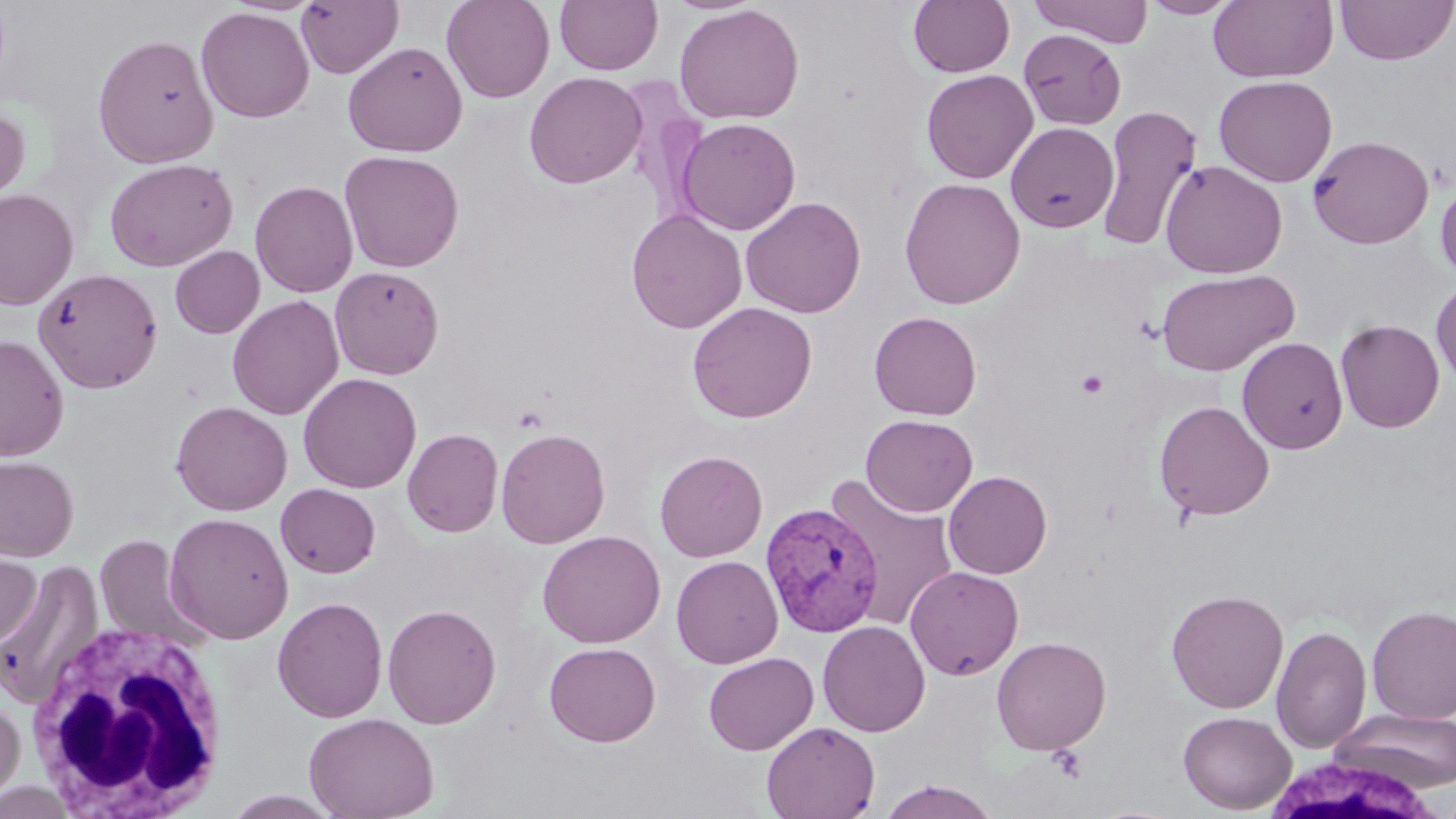
{
  "slide_level_diagnosis": "Plasmodium vivax",
  "uninfected_red_blood_cell_locations": "approximate bounding boxes as named x1/y1/x2/y2 corners in pixels: (x1=296, y1=0, x2=404, y2=79), (x1=441, y1=0, x2=554, y2=103), (x1=554, y1=0, x2=663, y2=75), (x1=908, y1=0, x2=1016, y2=78), (x1=1028, y1=0, x2=1153, y2=46), (x1=1138, y1=0, x2=1243, y2=19), (x1=1208, y1=0, x2=1338, y2=84), (x1=1334, y1=0, x2=1456, y2=66), (x1=674, y1=4, x2=804, y2=125), (x1=196, y1=8, x2=315, y2=123), (x1=1018, y1=28, x2=1126, y2=130), (x1=92, y1=33, x2=219, y2=168), (x1=343, y1=41, x2=468, y2=157), (x1=921, y1=68, x2=1038, y2=184), (x1=524, y1=71, x2=647, y2=189), (x1=1214, y1=75, x2=1337, y2=187), (x1=0, y1=101, x2=30, y2=211), (x1=1096, y1=104, x2=1202, y2=252), (x1=676, y1=117, x2=801, y2=236), (x1=1006, y1=121, x2=1119, y2=233), (x1=1307, y1=134, x2=1434, y2=249), (x1=339, y1=150, x2=464, y2=273), (x1=104, y1=157, x2=238, y2=272), (x1=1160, y1=159, x2=1287, y2=279), (x1=899, y1=177, x2=1026, y2=310), (x1=1435, y1=177, x2=1456, y2=285), (x1=250, y1=180, x2=359, y2=298), (x1=0, y1=188, x2=79, y2=310), (x1=740, y1=196, x2=866, y2=318), (x1=626, y1=209, x2=747, y2=334), (x1=170, y1=245, x2=265, y2=338), (x1=329, y1=265, x2=444, y2=380), (x1=34, y1=267, x2=162, y2=393), (x1=1156, y1=269, x2=1298, y2=377), (x1=1431, y1=280, x2=1456, y2=388), (x1=227, y1=295, x2=344, y2=420), (x1=687, y1=301, x2=818, y2=424), (x1=869, y1=311, x2=982, y2=420), (x1=1335, y1=318, x2=1445, y2=433), (x1=0, y1=334, x2=69, y2=460), (x1=1237, y1=336, x2=1348, y2=454), (x1=298, y1=372, x2=422, y2=493), (x1=170, y1=400, x2=293, y2=516), (x1=1154, y1=400, x2=1275, y2=521), (x1=861, y1=414, x2=978, y2=517), (x1=402, y1=427, x2=503, y2=537), (x1=495, y1=427, x2=610, y2=548), (x1=654, y1=450, x2=768, y2=562), (x1=0, y1=454, x2=79, y2=562), (x1=943, y1=471, x2=1052, y2=579), (x1=823, y1=474, x2=960, y2=631), (x1=275, y1=483, x2=381, y2=578), (x1=164, y1=512, x2=294, y2=644), (x1=537, y1=530, x2=666, y2=648), (x1=93, y1=534, x2=208, y2=650), (x1=0, y1=546, x2=41, y2=650), (x1=671, y1=555, x2=783, y2=668), (x1=1, y1=559, x2=104, y2=709), (x1=905, y1=565, x2=1024, y2=681), (x1=1166, y1=589, x2=1289, y2=713), (x1=272, y1=596, x2=389, y2=723), (x1=382, y1=603, x2=501, y2=729), (x1=1367, y1=605, x2=1456, y2=723), (x1=817, y1=620, x2=931, y2=737), (x1=1271, y1=625, x2=1371, y2=754), (x1=991, y1=636, x2=1111, y2=755), (x1=544, y1=642, x2=661, y2=747), (x1=703, y1=651, x2=819, y2=755), (x1=0, y1=693, x2=25, y2=808), (x1=1332, y1=708, x2=1456, y2=792), (x1=1178, y1=710, x2=1296, y2=814), (x1=304, y1=712, x2=439, y2=819), (x1=762, y1=721, x2=880, y2=819), (x1=876, y1=781, x2=1001, y2=818), (x1=223, y1=790, x2=343, y2=818)",
  "preparation": "thin blood smear",
  "white_blood_cell_locations": "approximate bounding boxes as named x1/y1/x2/y2 corners in pixels: (x1=26, y1=618, x2=230, y2=818), (x1=1258, y1=752, x2=1449, y2=819)",
  "image_size": "1456×819 pixels",
  "platelet_locations": "approximate bounding boxes as named x1/y1/x2/y2 corners in pixels: (x1=1075, y1=370, x2=1110, y2=398)",
  "field_of_view": "one of a larger specimen",
  "modality": "light microscopy",
  "stain": "May-Grünwald-Giemsa",
  "plasmodium_vivax_infected_red_blood_cell_locations": "approximate bounding boxes as named x1/y1/x2/y2 corners in pixels: (x1=761, y1=502, x2=884, y2=637)",
  "magnification": "1000x"
}